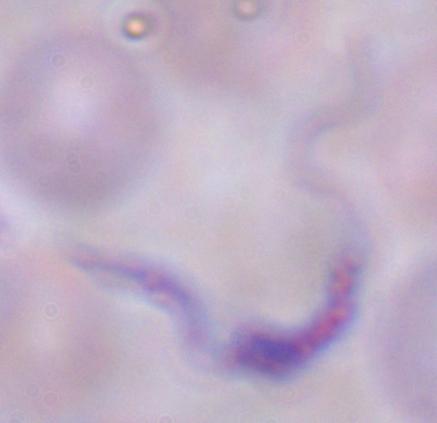

{
  "identification": "trypanosome",
  "modality": "photomicrograph",
  "magnification": "1000x"
}